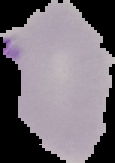
result = malaria parasites identified
preparation = thin blood film
image type = segmented cell region on a black background
image size = 115×163 pixels